Give the position of every Plasmodium parasite visible.
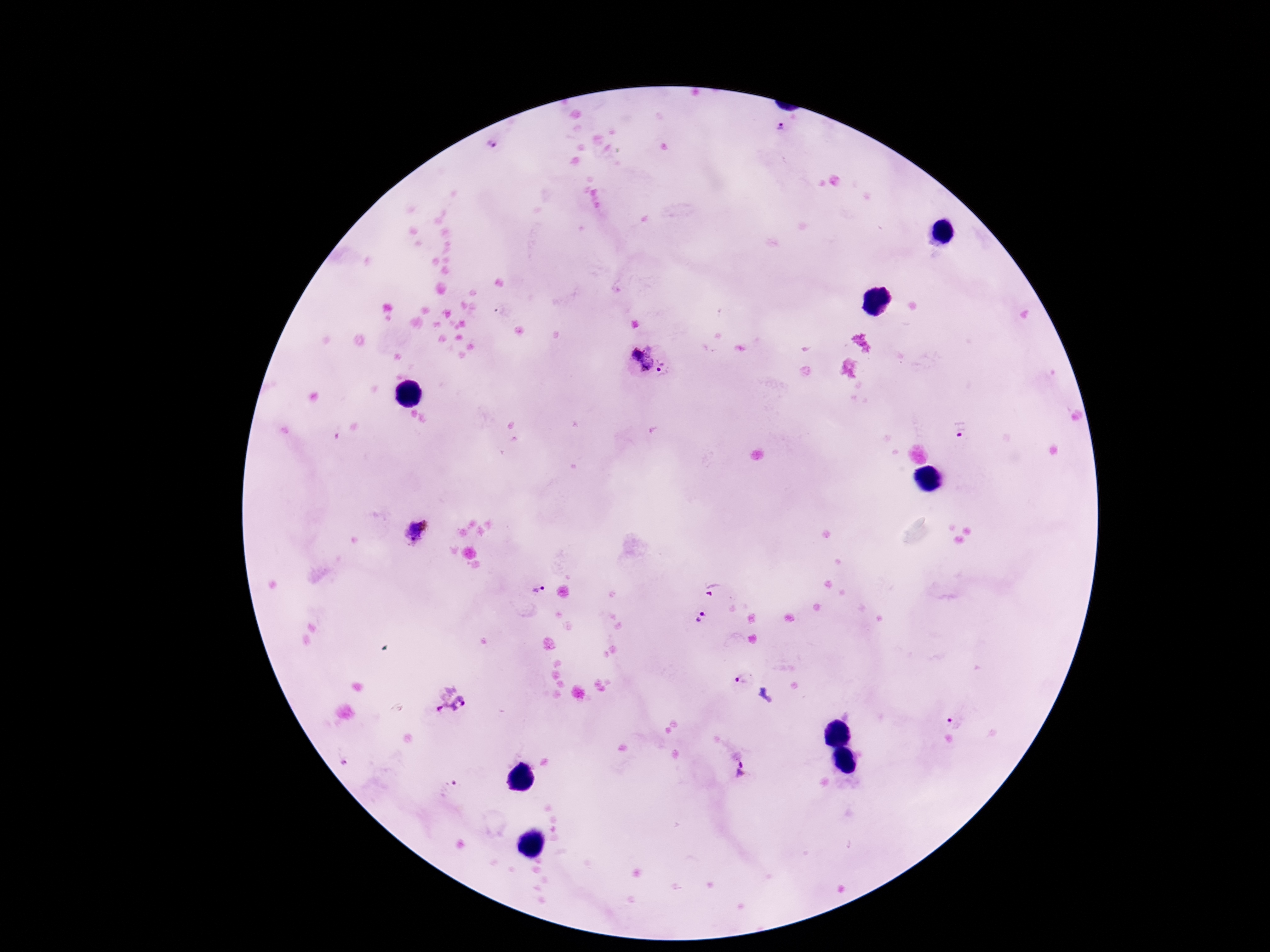
Approximate object centers, in pixels from the top-left corner.
Plasmodium parasites: (x=780, y=130), (x=488, y=147), (x=647, y=351), (x=637, y=354), (x=661, y=362), (x=646, y=365), (x=658, y=370), (x=960, y=432), (x=416, y=531), (x=535, y=587), (x=717, y=589), (x=700, y=615), (x=741, y=679), (x=450, y=697), (x=957, y=718), (x=742, y=774), (x=451, y=787).

Summary:
  - Patient malaria status: infected
  - Preparation: thick peripheral-blood smear
  - Stain: Giemsa
  - Magnification: 100x
  - Capture: smartphone camera through the microscope eyepiece
  - Field of view: one from this slide
  - Image size: 1270×952 pixels